Assess the morphology of the erythrocytes.
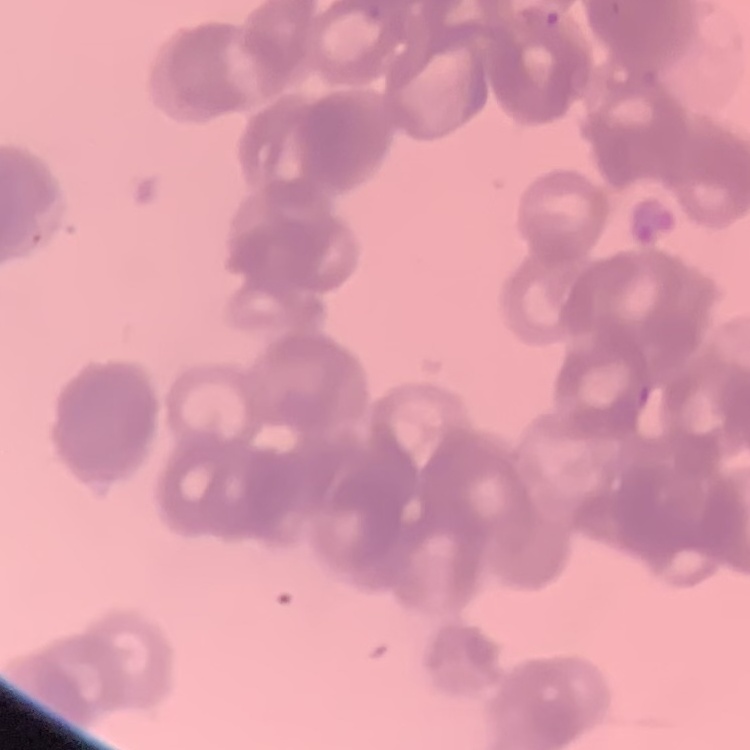
They show rouleaux formation.

Summary:
  - Image type: one tile cut from a larger photomicrograph
  - Preparation: thin blood film
  - Stain: Field's or Giemsa